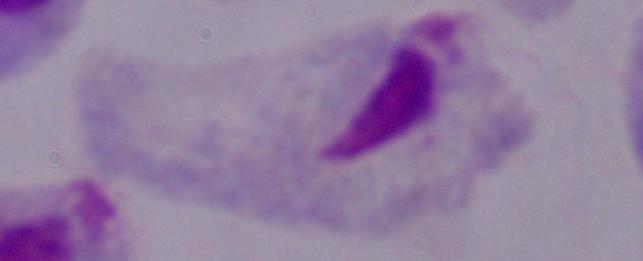
identification = trichomonad
modality = micrograph
magnification = 1000x